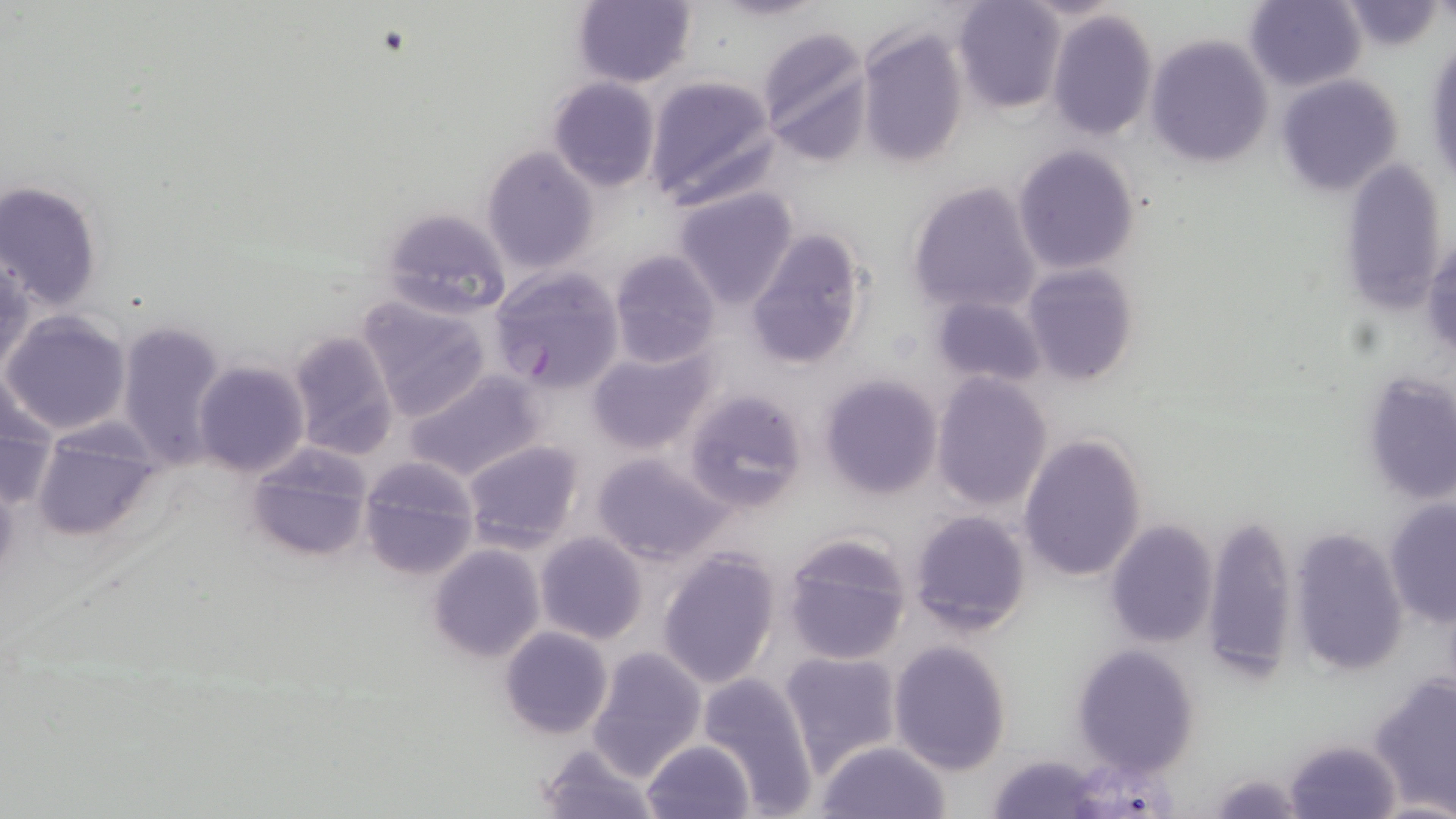
Approximate bounding boxes as [x1, y1, x2, y2] in pixels. Plasmodium falciparum-infected red blood cell locations: [490, 266, 624, 394]. Uninfected red blood cell locations: [1244, 0, 1366, 92], [570, 1, 696, 87], [953, 1, 1066, 114], [1338, 1, 1444, 51], [1047, 10, 1158, 140], [759, 27, 874, 163], [857, 27, 969, 169], [1425, 34, 1455, 194], [1146, 35, 1273, 169], [1275, 74, 1403, 196], [644, 76, 777, 208], [548, 77, 660, 191], [1012, 144, 1138, 274], [480, 147, 598, 276], [1341, 157, 1446, 314], [0, 180, 105, 313], [905, 181, 1042, 317], [673, 188, 799, 310], [376, 207, 513, 319], [745, 227, 870, 371], [1424, 233, 1455, 366], [609, 250, 721, 368], [0, 252, 32, 381], [1021, 263, 1139, 386], [929, 293, 1048, 388], [357, 295, 494, 423], [2, 310, 132, 437], [113, 320, 226, 468], [287, 330, 399, 460], [587, 349, 713, 455], [193, 360, 309, 478], [403, 368, 544, 482], [1360, 369, 1456, 507], [931, 372, 1052, 512], [818, 373, 943, 499], [0, 374, 57, 510], [683, 388, 809, 514], [30, 423, 161, 541], [1017, 431, 1147, 584], [461, 439, 584, 552], [247, 446, 373, 564], [591, 453, 728, 565], [358, 457, 481, 580], [1384, 499, 1456, 628], [908, 509, 1034, 636], [1203, 515, 1298, 684], [1103, 519, 1217, 649], [1288, 528, 1409, 676], [535, 532, 648, 644], [780, 533, 913, 665], [429, 545, 544, 662], [657, 548, 780, 688], [499, 626, 614, 738], [889, 641, 1012, 773], [1070, 645, 1200, 777], [586, 646, 705, 780], [779, 650, 904, 772], [698, 675, 819, 813], [1368, 675, 1456, 815], [1285, 737, 1399, 818], [641, 739, 758, 819], [815, 740, 952, 819], [535, 741, 659, 819], [988, 753, 1102, 819]. Slide-level diagnosis: Plasmodium falciparum. Light microscopy. May-Grünwald-Giemsa stain. Thin blood smear. Single field of view. Image is 1456×819 pixels. 1000x magnification.